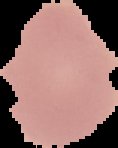
Summary:
  - Preparation: thin blood smear
  - Image type: segmented cell region on a black background
  - Image size: 118×148 pixels
  - Malaria status: uninfected